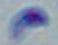
identification = Toxoplasma gondii
magnification = 1000x
modality = photomicrograph